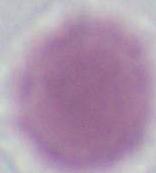

modality = micrograph
identification = red blood cell
magnification = 1000x